Classify this cell by malaria status.
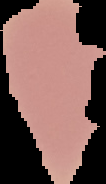
Uninfected.

Image is 106×184 pixels. From a thin blood smear. The area outside the segmented cell region is set to black.